Classify this cell by malaria status.
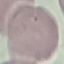
It is uninfected.

Automatically extracted cell patch, resized to 64 × 64 pixels. Thin blood film. Photographed with a smartphone camera at the microscope eyepiece. Giemsa-stained preparation.